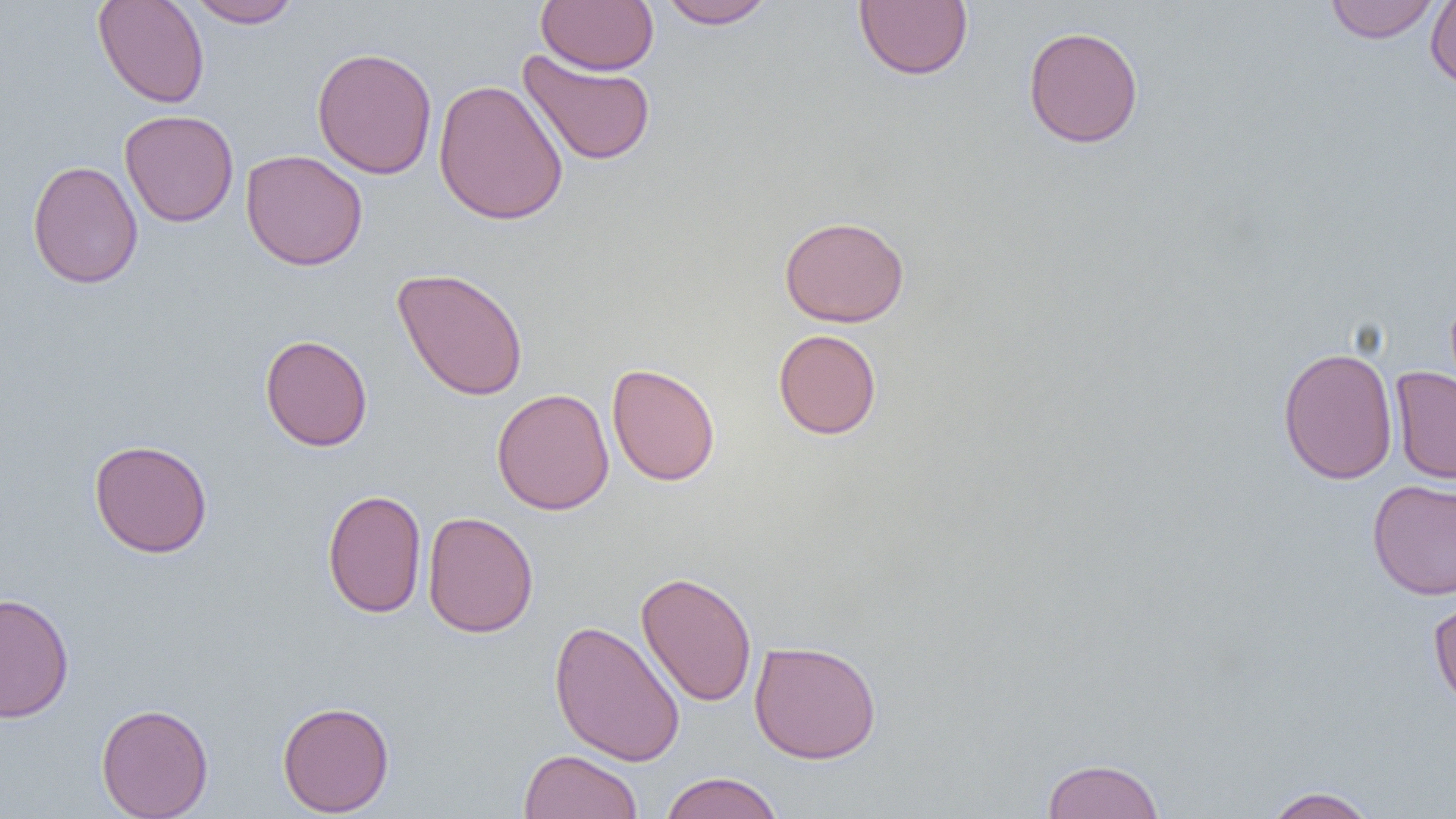 Approximate bounding boxes as (x1,y1)-(x2,y2) corner pairs in pixels. Uninfected red blood cell locations: (92,0)-(210,108), (187,0)-(301,28), (536,0)-(658,75), (658,0)-(776,29), (853,0)-(973,81), (1425,0)-(1456,90), (1324,1)-(1440,43), (1023,25)-(1144,148), (311,46)-(438,179), (517,49)-(656,166), (433,78)-(568,226), (119,110)-(239,227), (241,149)-(368,271), (27,160)-(143,289), (779,215)-(909,327), (391,267)-(529,401), (773,329)-(882,440), (259,334)-(373,451), (1277,346)-(1398,484), (607,363)-(720,486), (1390,366)-(1456,485), (492,388)-(615,515), (89,439)-(213,558), (1367,479)-(1456,600), (322,488)-(427,619), (422,511)-(539,638), (636,571)-(757,707), (0,592)-(74,723), (1427,593)-(1456,713), (548,618)-(686,768), (749,639)-(882,763), (277,700)-(395,817), (96,703)-(214,818), (519,749)-(643,819), (1041,757)-(1165,819), (659,771)-(785,819), (1262,786)-(1381,819). Slide-level diagnosis: no evidence of blood parasites. One field of a larger specimen. Light microscopy. Image is 1456×819 pixels. Thin blood film. 1000x magnification.